State which parasite is depicted.
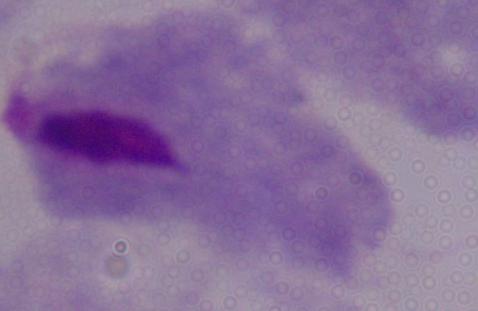

A trichomonad.

magnification = 1000x
modality = photomicrograph